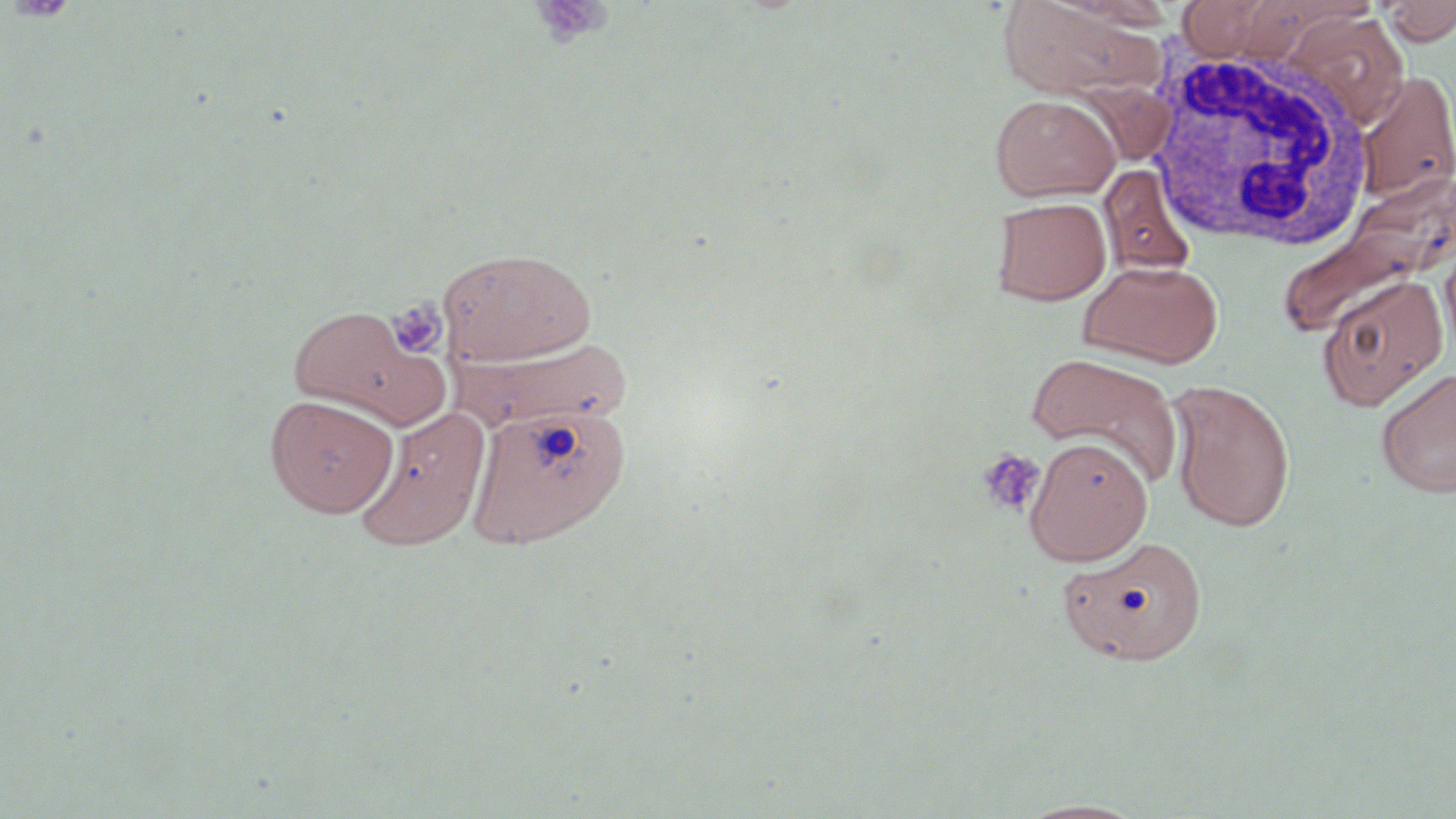

Summary:
  - Coordinate format: approximate bounding boxes as (x1,y1)-(x2,y2) corner pairs in pixels
  - Platelet locations: (5,0)-(79,23), (529,1)-(614,48), (388,299)-(448,359), (976,448)-(1046,518)
  - Uninfected red blood cell locations: (996,0)-(1155,100), (1175,0)-(1294,61), (1379,0)-(1456,45), (1285,10)-(1411,126), (1356,71)-(1456,203), (990,93)-(1120,202), (1099,164)-(1197,278), (991,196)-(1111,305), (1271,198)-(1445,341), (1440,234)-(1456,362), (436,247)-(598,367), (1079,260)-(1223,368), (1317,274)-(1449,411), (286,304)-(439,423), (452,337)-(634,434), (1027,352)-(1185,488), (1375,366)-(1456,498), (1165,378)-(1297,532), (264,393)-(398,518), (467,402)-(630,549), (353,406)-(491,552), (1024,437)-(1153,566), (1057,534)-(1206,667), (1015,798)-(1150,818)
  - White blood cell locations: (1145,43)-(1377,251)
  - Slide-level diagnosis: negative for blood parasites
  - Magnification: 1000x
  - Preparation: thin blood smear
  - Modality: light microscopy
  - Stain: May-Grünwald-Giemsa
  - Field of view: one of a larger specimen
  - Image size: 1456×819 pixels